Report the malaria status of this cell.
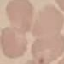

It is uninfected.

Thin blood smear. Cell patch, automatically extracted from a larger field of view and resized to 64 × 64 pixels. Giemsa-stained preparation. Acquired by smartphone through the microscope eyepiece.